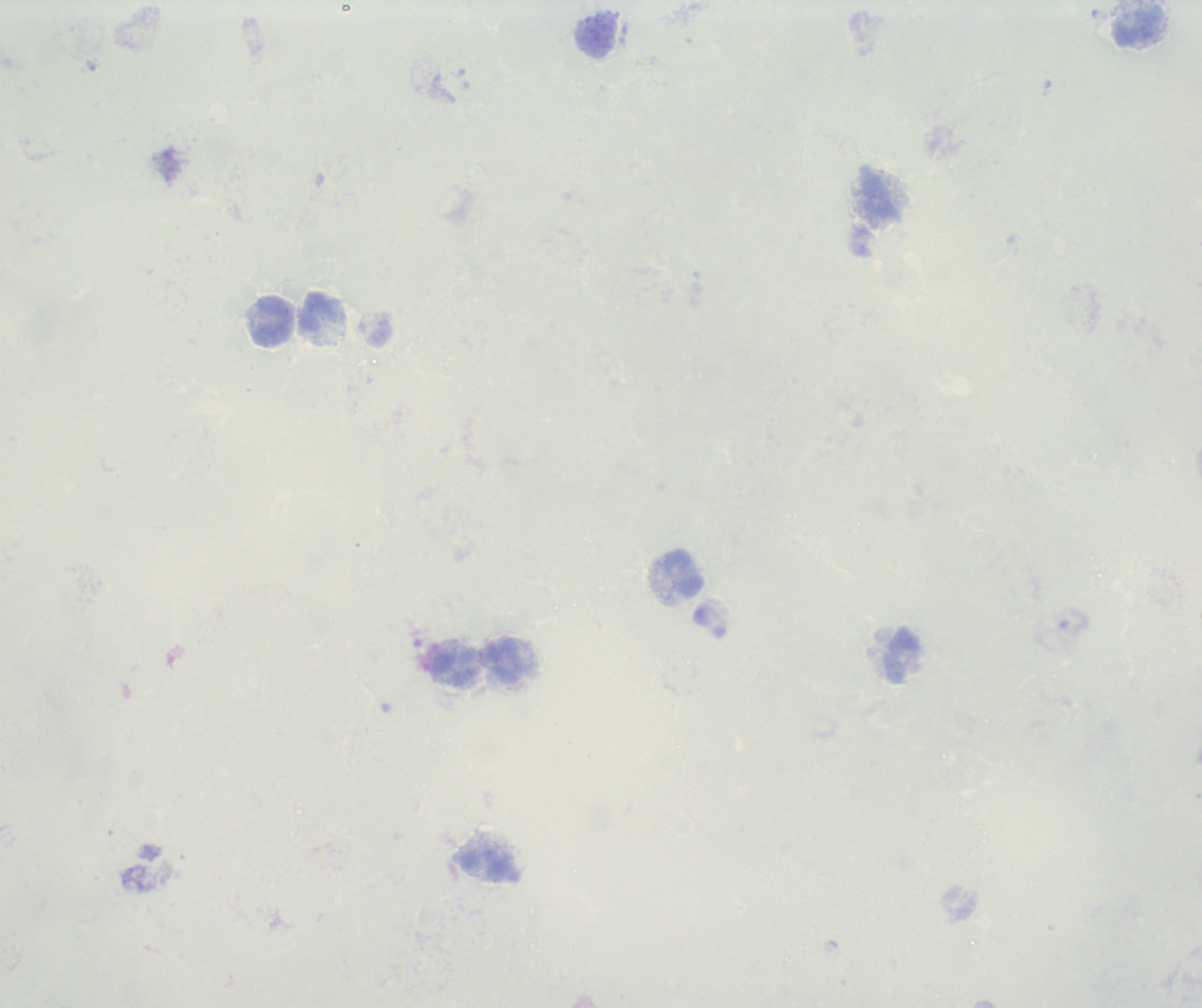
Approximate object centers, in pixels from the top-left corner. Leukocyte locations: (x=1138, y=27), (x=878, y=200), (x=320, y=312), (x=273, y=320), (x=683, y=574), (x=901, y=656), (x=505, y=662), (x=454, y=667), (x=487, y=863). Thick blood film. Result: no malaria parasites seen. 100x magnification. Previously used in an actual diagnosis. Romanowsky stain. Image is 1202×1008 pixels. Background quality: poor. Single field of view.